State which parasite is depicted.
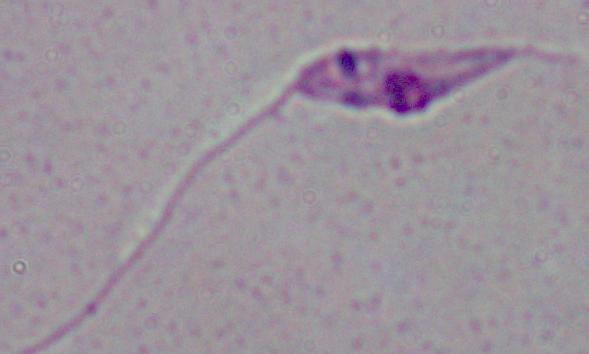

Leishmania.

modality = photomicrograph
magnification = 1000x